Describe the morphology of the red blood cells.
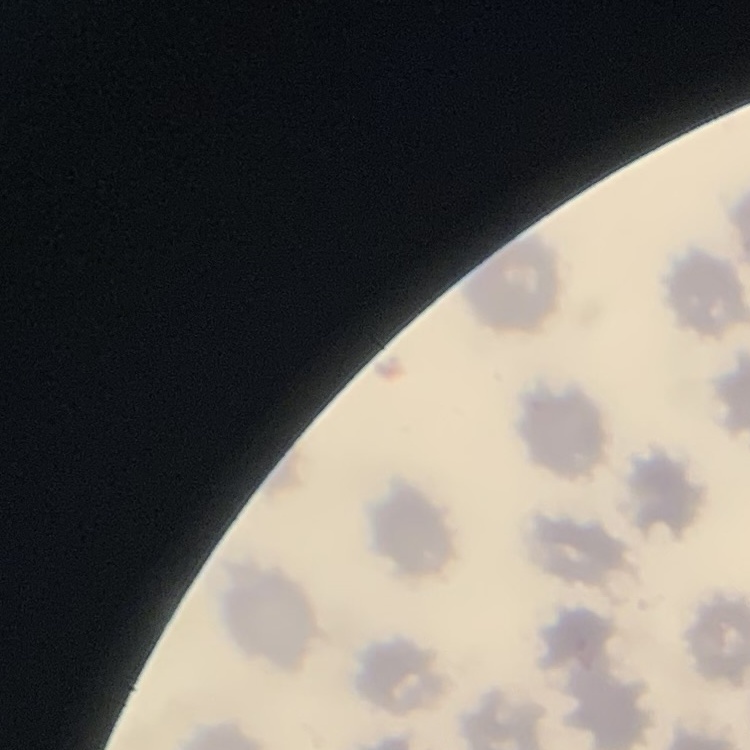

No rouleaux formation.

Thin blood smear. Stained with either Field's or Giemsa. One tile cut from a larger photomicrograph.